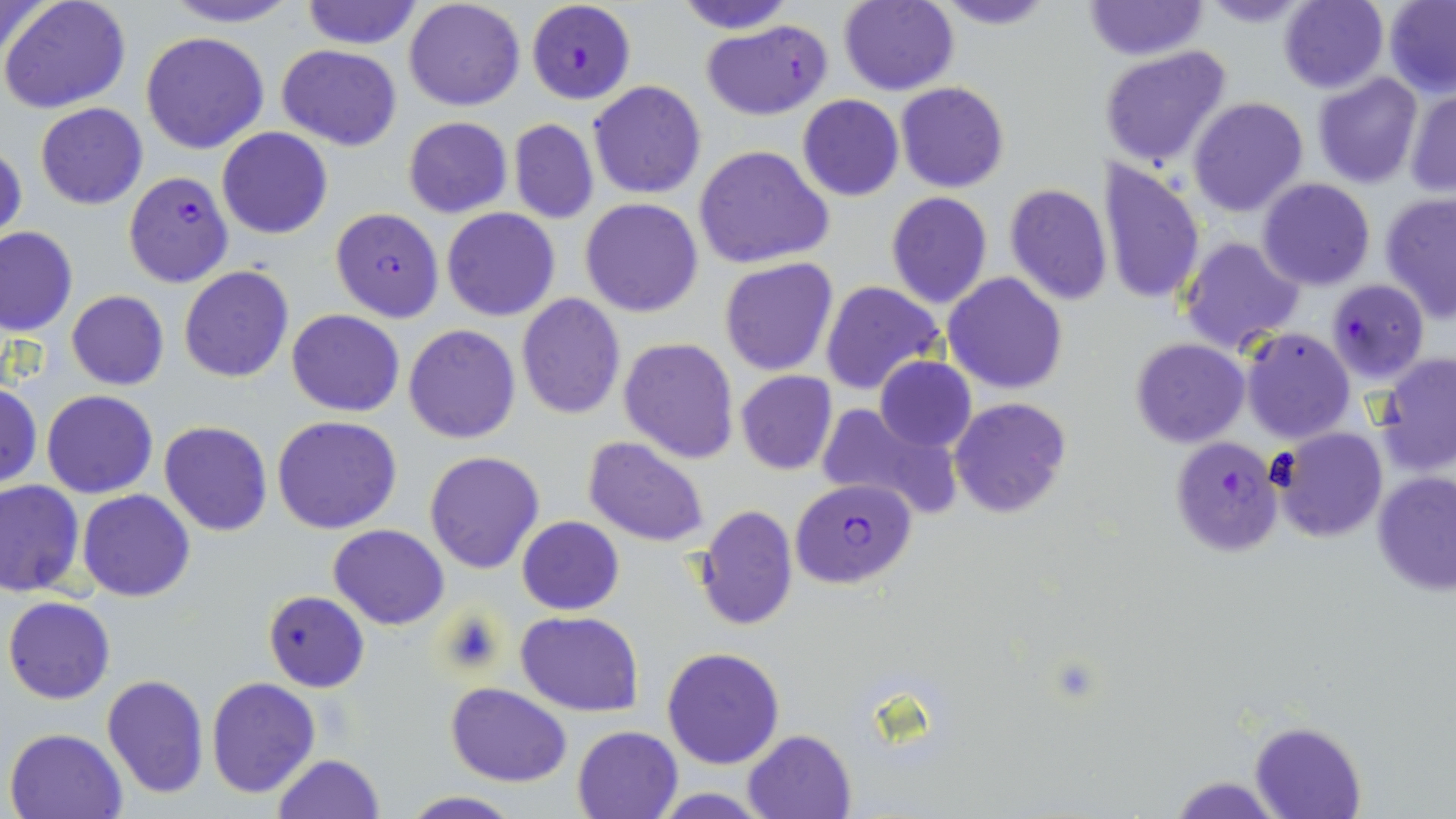

slide-level diagnosis = Plasmodium falciparum
stain = May-Grünwald-Giemsa
magnification = 1000x
Plasmodium falciparum-infected red blood cell locations = approximate bounding boxes as (x1,y1)-(x2,y2) corner pairs in pixels: (529,3)-(650,106), (701,19)-(834,120), (123,172)-(234,289), (331,207)-(444,321), (1325,278)-(1430,385), (1169,436)-(1282,558), (790,477)-(916,590)
field of view = one of a larger specimen
preparation = thin blood film
modality = optical microscopy
uninfected red blood cell locations = approximate bounding boxes as (x1,y1)-(x2,y2) corner pairs in pixels: (1,0)-(133,114), (158,0)-(304,28), (300,0)-(421,49), (403,0)-(527,112), (671,0)-(798,35), (928,0)-(1059,30), (1082,0)-(1207,60), (1196,0)-(1317,28), (1277,0)-(1388,91), (1,1)-(55,62), (838,1)-(959,96), (1384,1)-(1456,95), (141,31)-(270,154), (276,44)-(402,149), (1098,45)-(1234,172), (1312,73)-(1424,189), (588,81)-(708,200), (896,81)-(1009,194), (1404,89)-(1456,196), (797,94)-(904,201), (1188,97)-(1309,218), (35,102)-(148,209), (402,117)-(513,218), (508,118)-(599,225), (216,127)-(334,239), (0,142)-(25,248), (694,145)-(834,269), (1097,158)-(1205,306), (1256,177)-(1376,292), (1004,182)-(1113,305), (886,192)-(994,310), (1379,192)-(1456,322), (579,197)-(705,317), (440,207)-(560,321), (0,225)-(78,336), (1179,235)-(1306,356), (719,258)-(838,376), (178,266)-(295,383), (943,273)-(1067,394), (821,281)-(946,398), (65,290)-(169,390), (516,294)-(627,422), (287,309)-(404,416), (403,324)-(520,444), (1241,328)-(1354,443), (618,336)-(740,463), (1131,337)-(1250,448), (1375,354)-(1456,477), (873,357)-(976,453), (734,371)-(838,476), (0,383)-(42,488), (42,390)-(157,498), (948,397)-(1072,518), (814,402)-(958,518), (271,414)-(403,534), (158,421)-(273,536), (1274,428)-(1388,542), (583,437)-(711,548), (423,450)-(545,574), (1372,470)-(1456,595), (0,480)-(84,597), (78,489)-(194,601), (693,504)-(798,632), (517,516)-(624,615), (329,524)-(449,630), (264,591)-(369,692), (3,596)-(115,704), (515,610)-(644,714), (661,646)-(785,769), (101,674)-(209,799), (206,677)-(321,799), (446,681)-(573,787), (1249,721)-(1365,819), (572,724)-(684,818), (4,727)-(128,819), (742,729)-(856,818), (271,754)-(385,819), (1170,776)-(1282,817), (649,789)-(779,818), (400,792)-(523,819)
image size = 1456×819 pixels